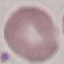
Summary:
  - Malaria status: uninfected
  - Preparation: thin blood smear
  - Capture: smartphone through the microscope eyepiece
  - Image type: cell patch, automatically extracted from a larger field of view and resized to 64 × 64 pixels
  - Stain: Giemsa